Report the malaria status of this cell.
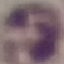

Uninfected.

Summary:
  - Capture: smartphone through the microscope eyepiece
  - Stain: Giemsa
  - Image type: automatically extracted cell patch, resized to 64 × 64 pixels
  - Preparation: thin blood film